Assess this cell for malaria.
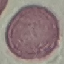
It is uninfected.

Summary:
  - Preparation: thin blood film
  - Capture: smartphone camera at the microscope eyepiece
  - Stain: Giemsa
  - Image type: cell patch, automatically extracted from a larger field of view and resized to 64 × 64 pixels